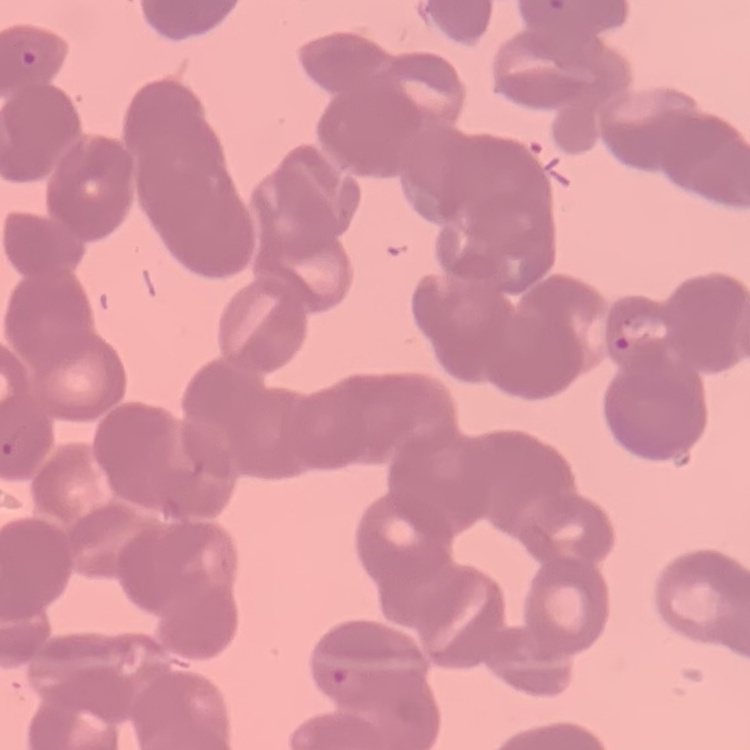

erythrocyte morphology = rouleaux formation
preparation = thin blood smear
stain = Field's or Giemsa
image type = square crop of a larger photomicrograph